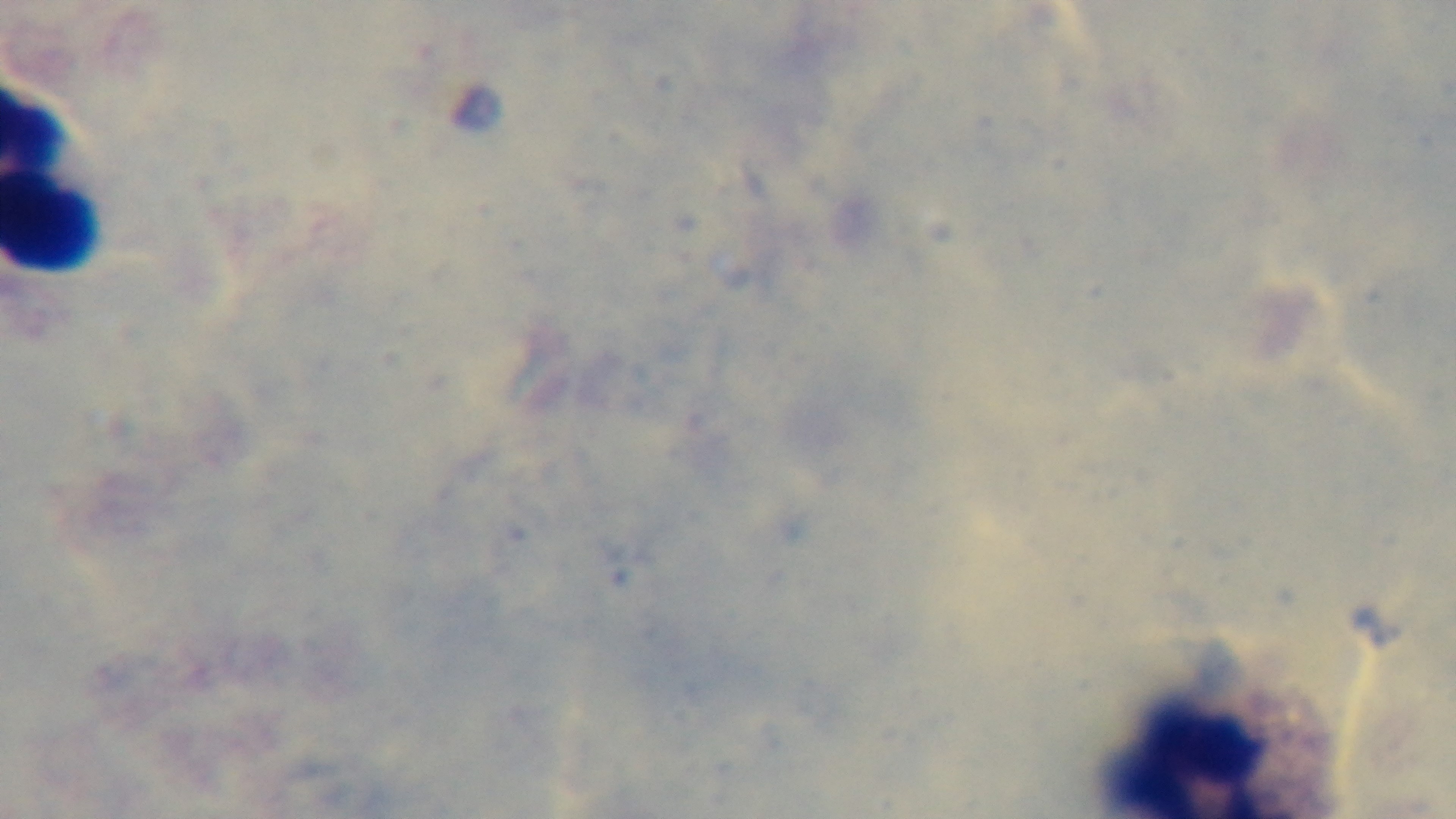

Summary:
  - Field of view: single
  - Preparation: thick
  - Modality: light microscopy
  - Stain: Giemsa
  - Capture: mounted 4K digital camera
  - Objective: 100x oil immersion
  - Malaria status: uninfected